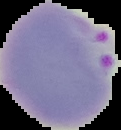

{
  "result": "malaria parasites identified",
  "image_size": "121×130 pixels",
  "preparation": "thin blood film",
  "image_type": "segmented cell region with the area outside set to black"
}